Classify this cell by malaria status.
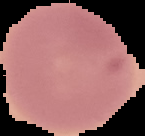
It is uninfected.

Image is 145×136 pixels. From a thin blood film. The area outside the segmented cell region is set to black.